Report the malaria status of this cell.
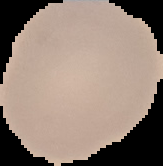
It is uninfected.

image size = 163×166 pixels
image type = cell region segmented out of the field of view; surrounding area masked to black
preparation = thin blood smear